Give a bounding box for every leukocyte visible.
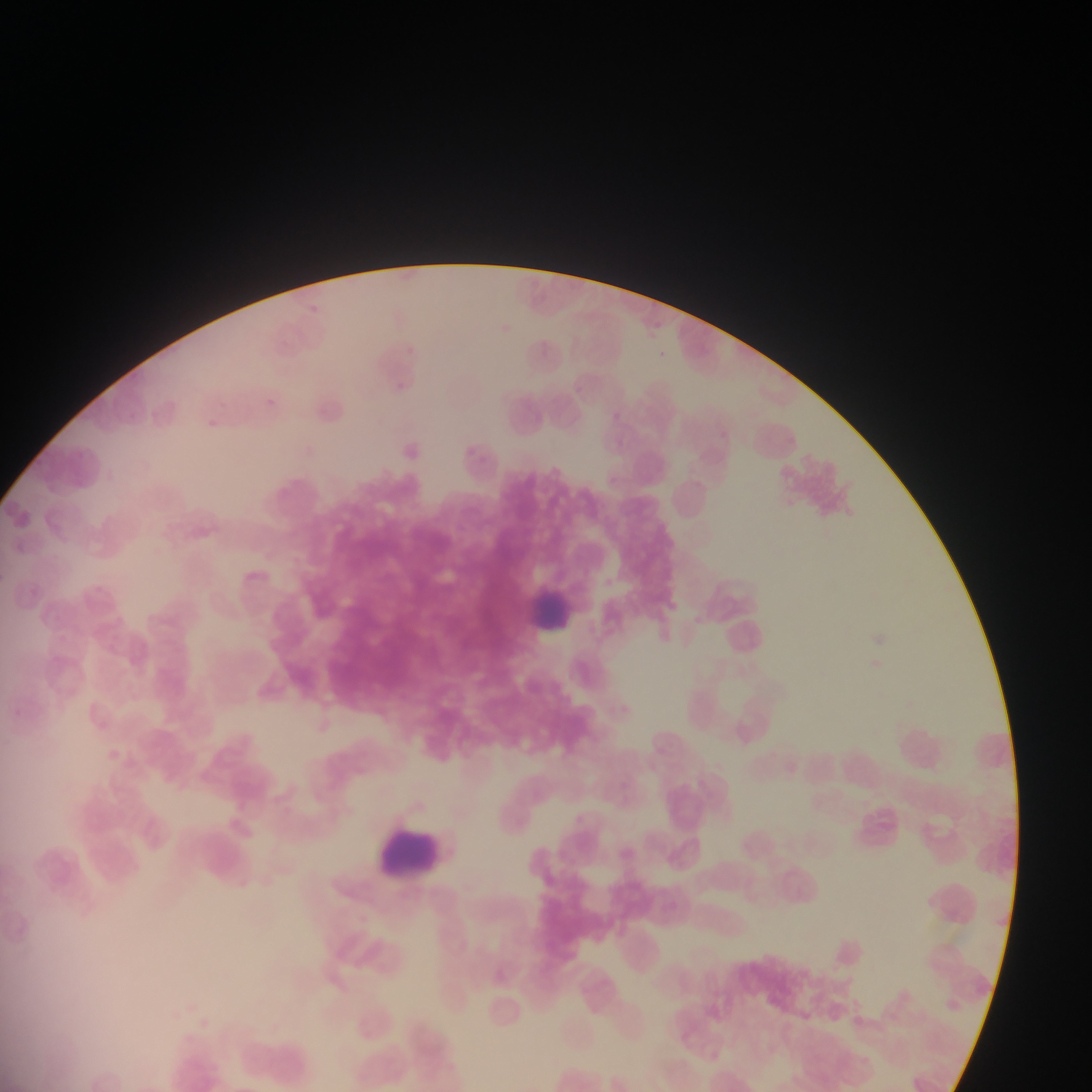

Approximate bounding boxes as left top right bottom in pixels.
Leukocytes: 520 578 586 644; 372 827 441 903.

field of view = single
capture = mobile-phone photograph through a microscope
country = Ghana
image size = 1092×1092 pixels
preparation = thin blood film